Classify this cell by malaria status.
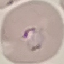

Parasitized.

Giemsa stain. Photographed with a smartphone camera at the microscope eyepiece. Automatically extracted cell patch, resized to 64 × 64 pixels. Thin blood smear.